Identify the parasite.
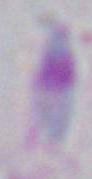

This is Toxoplasma gondii.

Photomicrograph. Captured at 1000x magnification.